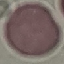 Malaria status: uninfected. Giemsa-stained preparation. Thin smear of blood. Automatically extracted cell patch, resized to 64 × 64 pixels. Acquired by smartphone through the microscope eyepiece.